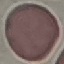

Malaria status: uninfected. Giemsa-stained preparation. Cell patch, automatically extracted from a larger field of view and resized to 64 × 64 pixels. Acquired by smartphone through the microscope eyepiece. Thin smear of blood.